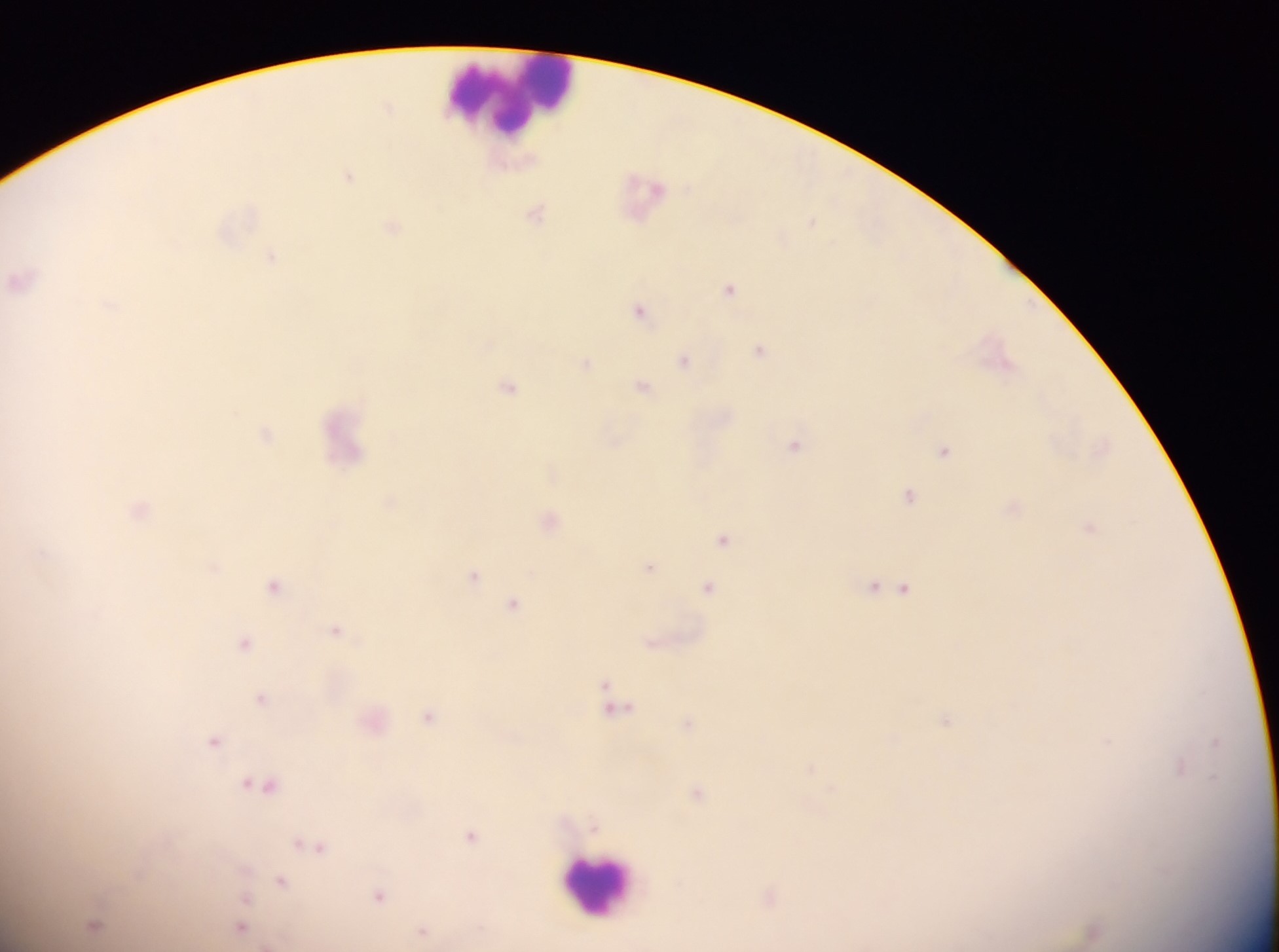

capture: mobile-phone photograph through a microscope
leukocyte_locations: 'approximate centers as x y in pixels: 515 97; 599 884'
image_size: 1279×952 pixels
country: Ghana
field_of_view: single
plasmodium_parasite_locations: 'approximate centers as x y in pixels: 388 106; 349 177; 536 213; 812 221; 392 227; 271 257; 21 280; 730 289; 640 310; 760 350; 685 360; 586 363; 643 386; 509 387; 265 434; 795 445; 943 451; 909 495; 140 509; 1090 528; 723 539; 215 567; 649 567; 474 575; 275 586; 709 586; 874 586; 903 588; 514 604; 336 630; 245 643; 263 697; 614 702; 429 715; 945 720; 688 722; 215 740; 1215 741; 1180 766; 811 767; 262 785; 698 792; 471 835; 313 845; 282 881; 379 895; 769 895; 245 898; 94 924; 240 928; 424 930; 1093 931'
preparation: thick blood smear